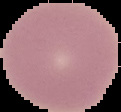 Image is 121×112 pixels. From a thin blood smear. Result: no Plasmodium parasites seen. Segmented cell region on a black background.